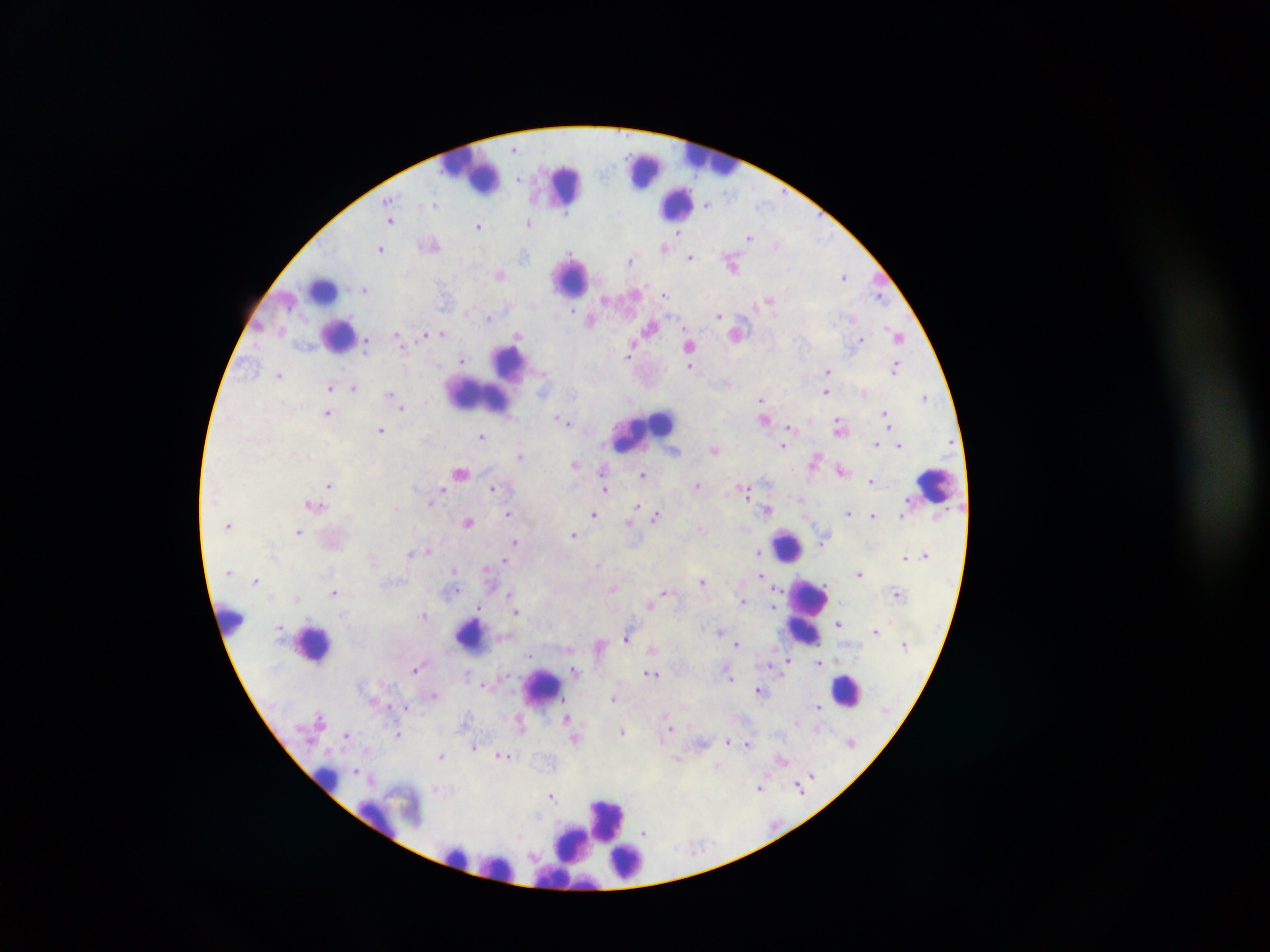

Approximate centers as {x, y} in pixels.
Summary:
  - Plasmodium parasite locations: {513, 148}, {540, 170}, {521, 176}, {519, 177}, {390, 198}, {708, 203}, {434, 204}, {568, 214}, {391, 222}, {527, 224}, {479, 227}, {677, 231}, {821, 236}, {751, 238}, {777, 243}, {663, 247}, {380, 248}, {571, 254}, {687, 254}, {525, 255}, {690, 258}, {629, 259}, {498, 275}, {845, 276}, {641, 287}, {364, 288}, {664, 295}, {880, 298}, {606, 299}, {769, 299}, {573, 310}, {466, 312}, {718, 315}, {488, 319}, {850, 319}, {591, 320}, {886, 329}, {441, 332}, {517, 335}, {422, 336}, {397, 337}, {861, 337}, {899, 337}, {367, 344}, {632, 348}, {629, 355}, {463, 358}, {895, 367}, {691, 368}, {828, 371}, {278, 375}, {328, 386}, {354, 386}, {826, 392}, {389, 393}, {924, 398}, {761, 400}, {763, 403}, {401, 407}, {884, 412}, {326, 415}, {558, 419}, {888, 420}, {567, 421}, {790, 426}, {380, 430}, {482, 435}, {876, 443}, {783, 447}, {899, 447}, {715, 450}, {521, 455}, {815, 460}, {576, 465}, {602, 469}, {461, 473}, {644, 475}, {330, 485}, {698, 485}, {494, 487}, {606, 488}, {442, 490}, {747, 490}, {799, 499}, {432, 501}, {637, 504}, {311, 505}, {767, 511}, {847, 511}, {592, 513}, {509, 514}, {655, 516}, {468, 521}, {629, 522}, {298, 532}, {574, 536}, {823, 539}, {515, 542}, {427, 552}, {757, 553}, {410, 554}, {907, 556}, {504, 561}, {599, 564}, {454, 569}, {487, 569}, {226, 574}, {761, 575}, {858, 575}, {703, 579}, {256, 580}, {613, 588}, {663, 591}, {334, 592}, {510, 592}, {777, 592}, {448, 594}, {899, 595}, {297, 597}, {742, 599}, {650, 603}, {775, 607}, {479, 610}, {424, 614}, {518, 614}, {346, 616}, {837, 623}, {717, 632}, {875, 632}, {626, 638}, {904, 642}, {738, 644}, {653, 650}, {529, 656}, {788, 659}, {819, 662}, {772, 666}, {416, 669}, {576, 670}, {650, 674}, {656, 676}, {731, 676}, {483, 685}, {757, 690}, {434, 695}, {614, 699}, {564, 701}, {818, 706}, {409, 708}, {821, 711}, {319, 716}, {566, 719}, {797, 723}, {669, 728}, {819, 728}, {623, 732}, {346, 736}, {399, 736}, {576, 741}, {726, 741}, {747, 743}, {473, 748}, {501, 756}, {441, 757}, {507, 757}, {512, 757}, {679, 759}, {784, 760}, {718, 767}, {356, 770}, {359, 773}, {812, 773}, {798, 785}, {758, 788}, {433, 790}, {799, 790}, {551, 797}, {643, 832}
  - Leukocyte locations: {716, 163}, {641, 170}, {472, 176}, {569, 186}, {674, 199}, {564, 278}, {321, 293}, {335, 334}, {517, 365}, {479, 396}, {662, 423}, {621, 440}, {933, 487}, {786, 544}, {814, 597}, {229, 619}, {804, 634}, {471, 637}, {310, 645}, {849, 689}, {545, 694}, {323, 778}, {611, 818}, {373, 820}, {572, 845}, {458, 855}, {627, 862}, {499, 868}
  - Capture: mobile-phone photograph through a microscope
  - Field of view: single
  - Country: Ghana
  - Image size: 1270×952 pixels
  - Preparation: thick blood film